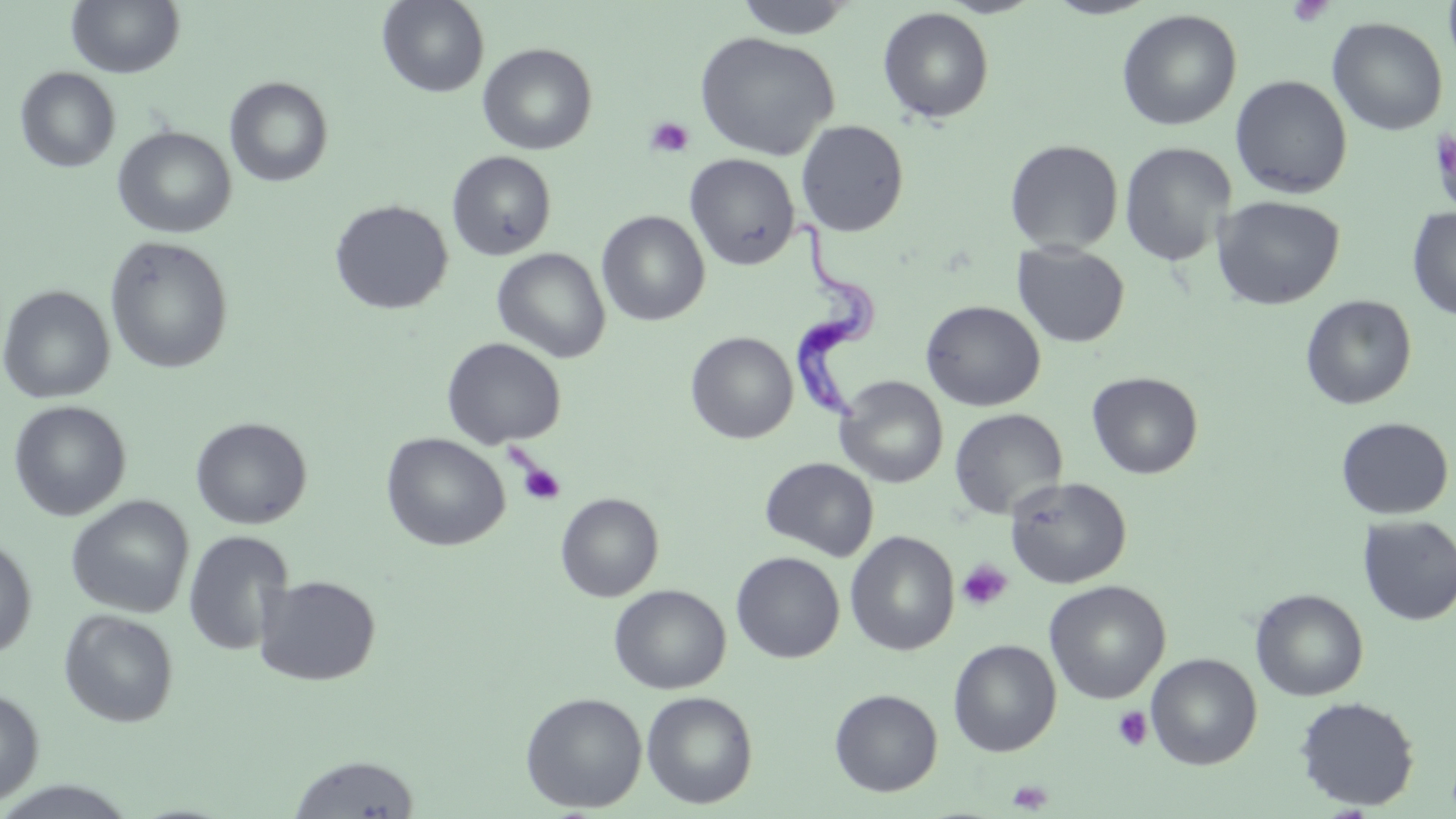
slide_level_diagnosis: Trypanosoma brucei
stain: May-Grünwald-Giemsa
platelet_locations: 'approximate bounding boxes as [x1, y1, x2, y2] in pixels: [1287, 0, 1334, 28], [645, 116, 695, 158], [517, 461, 566, 506], [956, 559, 1013, 612], [1112, 706, 1152, 751], [1006, 779, 1053, 813]'
uninfected_red_blood_cell_locations: 'approximate bounding boxes as [x1, y1, x2, y2] in pixels: [67, 0, 185, 78], [377, 0, 489, 98], [734, 0, 860, 39], [877, 6, 995, 124], [1116, 8, 1242, 131], [1327, 16, 1448, 135], [694, 31, 840, 161], [478, 43, 598, 155], [15, 67, 120, 173], [1230, 75, 1353, 199], [224, 77, 334, 187], [795, 120, 909, 236], [1431, 124, 1456, 219], [113, 126, 236, 238], [1004, 139, 1124, 253], [1119, 141, 1237, 266], [447, 151, 557, 261], [685, 153, 800, 270], [1211, 195, 1345, 310], [329, 199, 453, 315], [1407, 208, 1456, 321], [597, 211, 710, 326], [105, 236, 234, 374], [1012, 242, 1130, 348], [492, 248, 611, 363], [0, 284, 115, 404], [1300, 295, 1417, 410], [921, 300, 1046, 411], [685, 331, 798, 444], [442, 337, 566, 449], [1086, 371, 1203, 479], [835, 376, 948, 487], [8, 400, 131, 520], [949, 408, 1068, 520], [190, 416, 312, 529], [1336, 416, 1453, 520], [381, 433, 510, 551], [759, 457, 878, 561], [1005, 476, 1132, 589], [555, 492, 664, 602], [66, 495, 194, 618], [1357, 514, 1456, 625], [183, 530, 295, 656], [844, 531, 960, 656], [0, 533, 37, 660], [731, 552, 845, 663], [255, 575, 381, 686], [1044, 580, 1171, 704], [609, 584, 731, 694], [1250, 588, 1369, 701], [59, 609, 179, 727], [948, 638, 1062, 757], [1146, 653, 1262, 770], [0, 686, 44, 806], [829, 688, 943, 796], [520, 691, 647, 813], [641, 691, 758, 809], [1294, 696, 1420, 811], [288, 753, 421, 818], [0, 780, 141, 819]'
preparation: thin blood film
field_of_view: single
magnification: 1000x
modality: light microscopy
trypanosoma_brucei_locations: 'approximate bounding boxes as [x1, y1, x2, y2] in pixels: [788, 221, 882, 425]'
image_size: 1456×819 pixels